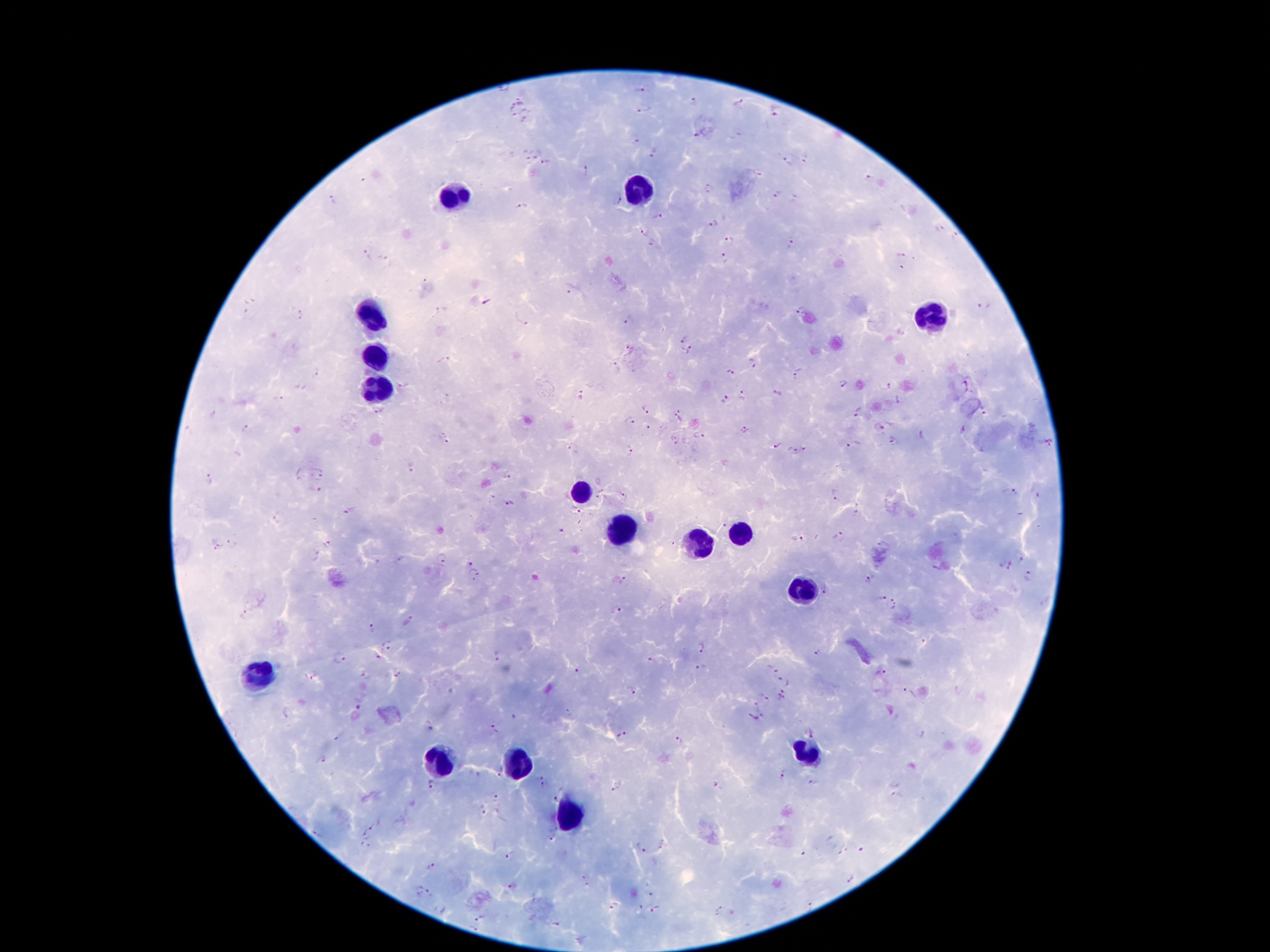
coordinate format = approximate object centers, in pixels from the top-left corner
malaria parasite locations = (x=502, y=89), (x=641, y=90), (x=521, y=99), (x=694, y=102), (x=738, y=103), (x=513, y=107), (x=644, y=109), (x=526, y=111), (x=778, y=112), (x=514, y=117), (x=524, y=119), (x=694, y=136), (x=634, y=143), (x=529, y=154), (x=539, y=154), (x=655, y=155), (x=805, y=159), (x=787, y=161), (x=546, y=163), (x=586, y=171), (x=869, y=178), (x=363, y=180), (x=709, y=188), (x=775, y=193), (x=618, y=198), (x=332, y=199), (x=521, y=207), (x=658, y=217), (x=714, y=224), (x=939, y=227), (x=643, y=232), (x=954, y=237), (x=729, y=240), (x=792, y=242), (x=652, y=243), (x=367, y=255), (x=902, y=255), (x=383, y=258), (x=724, y=258), (x=569, y=290), (x=487, y=303), (x=986, y=306), (x=299, y=309), (x=437, y=311), (x=801, y=311), (x=521, y=318), (x=629, y=321), (x=683, y=338), (x=630, y=347), (x=690, y=350), (x=444, y=360), (x=754, y=361), (x=614, y=366), (x=316, y=372), (x=731, y=373), (x=798, y=373), (x=844, y=383), (x=403, y=385), (x=888, y=386), (x=779, y=394), (x=744, y=395), (x=582, y=396), (x=276, y=397), (x=898, y=399), (x=724, y=400), (x=645, y=407), (x=984, y=410), (x=377, y=412), (x=678, y=412), (x=858, y=412), (x=213, y=414), (x=631, y=420), (x=648, y=427), (x=879, y=427), (x=246, y=428), (x=745, y=429), (x=699, y=435), (x=445, y=438), (x=675, y=441), (x=893, y=442), (x=777, y=444), (x=853, y=444), (x=1048, y=444), (x=805, y=447), (x=572, y=448), (x=630, y=450), (x=792, y=451), (x=412, y=468), (x=298, y=473), (x=319, y=476), (x=507, y=476), (x=207, y=480), (x=313, y=490), (x=1012, y=491), (x=835, y=492), (x=509, y=505), (x=349, y=509), (x=857, y=509), (x=278, y=515), (x=560, y=533), (x=838, y=536), (x=797, y=538), (x=232, y=543), (x=327, y=543), (x=217, y=548), (x=315, y=555), (x=442, y=557), (x=400, y=559), (x=1022, y=561), (x=469, y=562), (x=1011, y=567), (x=473, y=574), (x=1030, y=577), (x=868, y=580), (x=621, y=581), (x=827, y=589), (x=880, y=600), (x=896, y=605), (x=616, y=611), (x=244, y=614), (x=408, y=620), (x=374, y=629), (x=389, y=645), (x=702, y=647), (x=817, y=652), (x=379, y=654), (x=496, y=656), (x=339, y=659), (x=652, y=661), (x=774, y=669), (x=578, y=670), (x=701, y=670), (x=880, y=673), (x=396, y=674), (x=365, y=675), (x=308, y=677), (x=782, y=679), (x=631, y=691), (x=908, y=693), (x=764, y=694), (x=782, y=696), (x=757, y=704), (x=360, y=707), (x=285, y=711), (x=570, y=711), (x=762, y=716), (x=751, y=719), (x=429, y=723), (x=494, y=729), (x=810, y=732), (x=624, y=735), (x=337, y=738), (x=678, y=740), (x=322, y=760), (x=499, y=771), (x=782, y=772), (x=540, y=777), (x=714, y=783), (x=811, y=783), (x=543, y=785), (x=617, y=785), (x=430, y=786), (x=557, y=793), (x=895, y=795), (x=496, y=797), (x=481, y=811), (x=374, y=825), (x=318, y=833), (x=365, y=833), (x=553, y=835), (x=364, y=847), (x=640, y=848), (x=510, y=854), (x=431, y=867), (x=429, y=893), (x=809, y=903), (x=612, y=907), (x=720, y=908), (x=655, y=910), (x=480, y=917), (x=474, y=927)
leukocyte locations = (x=642, y=188), (x=453, y=194), (x=371, y=316), (x=935, y=318), (x=377, y=354), (x=377, y=385), (x=581, y=492), (x=621, y=530), (x=738, y=534), (x=698, y=540), (x=803, y=589), (x=258, y=675), (x=807, y=750), (x=520, y=759), (x=440, y=765), (x=574, y=813)
preparation = thick blood film
image size = 1270×952 pixels
stain = Giemsa
capture = smartphone camera through the microscope eyepiece
field of view = single
magnification = 100x
patient malaria status = positive for Plasmodium falciparum